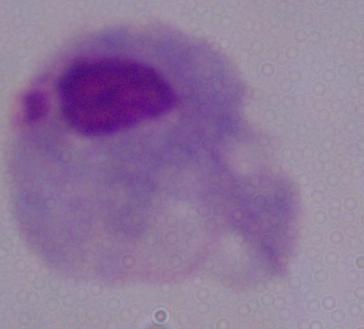
{
  "magnification": "1000x",
  "modality": "micrograph",
  "identification": "trichomonad"
}